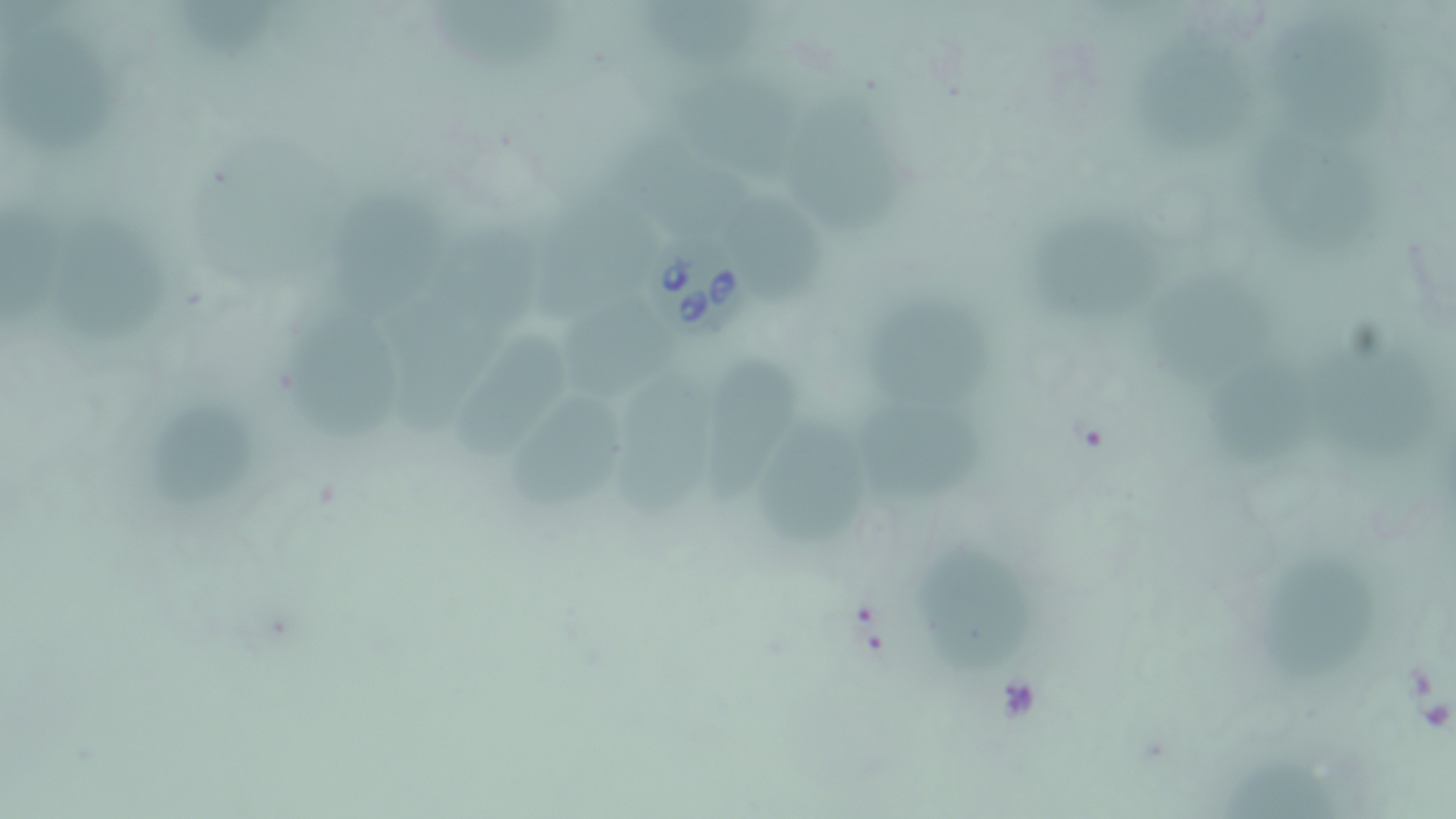
Summary:
  - Coordinate format: approximate bounding boxes as named x1/y1/x2/y2 corners in pixels
  - Uninfected red blood cell locations: (x1=426, y1=0, x2=571, y2=74), (x1=647, y1=2, x2=771, y2=64), (x1=186, y1=3, x2=294, y2=61), (x1=1270, y1=21, x2=1396, y2=139), (x1=1, y1=26, x2=131, y2=152), (x1=1137, y1=34, x2=1256, y2=156), (x1=665, y1=54, x2=804, y2=170), (x1=795, y1=92, x2=916, y2=242), (x1=1255, y1=135, x2=1385, y2=262), (x1=637, y1=143, x2=756, y2=222), (x1=332, y1=192, x2=446, y2=320), (x1=538, y1=194, x2=656, y2=318), (x1=736, y1=195, x2=827, y2=302), (x1=4, y1=200, x2=72, y2=333), (x1=62, y1=200, x2=170, y2=349), (x1=1039, y1=215, x2=1166, y2=317), (x1=441, y1=223, x2=563, y2=316), (x1=1161, y1=273, x2=1283, y2=373), (x1=871, y1=294, x2=1007, y2=414), (x1=564, y1=298, x2=697, y2=403), (x1=385, y1=309, x2=512, y2=440), (x1=290, y1=316, x2=406, y2=452), (x1=464, y1=334, x2=568, y2=466), (x1=1311, y1=341, x2=1426, y2=464), (x1=697, y1=352, x2=808, y2=506), (x1=1192, y1=357, x2=1299, y2=460), (x1=618, y1=365, x2=717, y2=514), (x1=843, y1=373, x2=983, y2=506), (x1=501, y1=387, x2=634, y2=523), (x1=150, y1=399, x2=261, y2=509), (x1=770, y1=412, x2=866, y2=537), (x1=916, y1=536, x2=1024, y2=671), (x1=1247, y1=560, x2=1375, y2=678), (x1=1224, y1=747, x2=1346, y2=818)
  - Babesia divergens-infected red blood cell locations: (x1=653, y1=234, x2=761, y2=341)
  - Slide-level diagnosis: Babesia divergens
  - Stain: May-Grünwald-Giemsa
  - Image size: 1456×819 pixels
  - Field of view: one of a larger specimen
  - Modality: light microscopy
  - Preparation: thin blood smear
  - Magnification: 1000x